Classify this cell by malaria status.
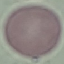

Uninfected.

Summary:
  - Preparation: thin blood film
  - Stain: Giemsa
  - Image type: cell patch, automatically extracted from a larger field of view and resized to 64 × 64 pixels
  - Capture: smartphone through the microscope eyepiece